Classify this cell by malaria status.
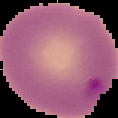
Parasitized.

Summary:
  - Image size: 118×118 pixels
  - Image type: segmented cell region with the area outside set to black
  - Preparation: thin blood film